Locate Plasmodium parasites and leukocytes.
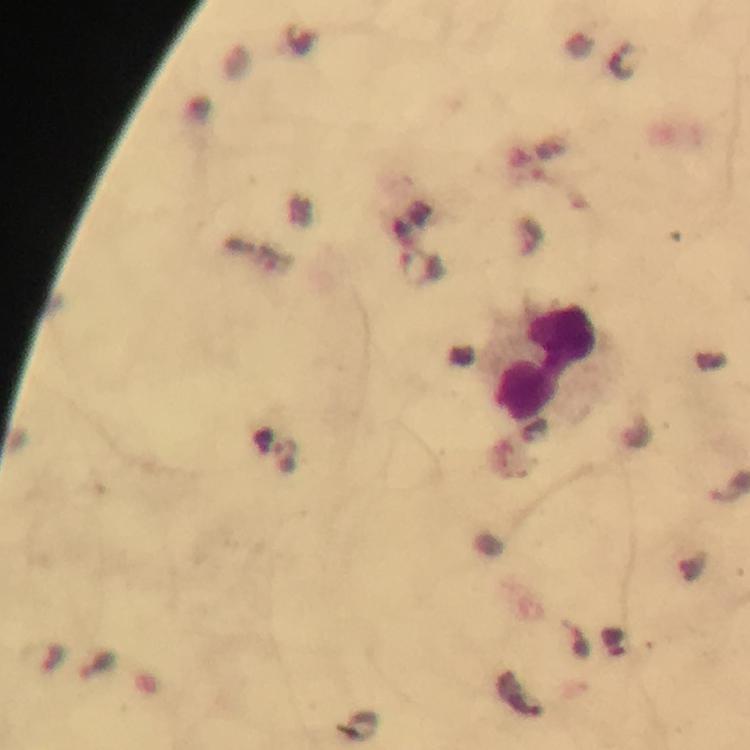
No Plasmodium parasites detected.
Approximate centers as {x, y} in pixels.
Leukocytes: {548, 363}.

Summary:
  - Context: from a malaria diagnostic workup
  - Immersion oil: used
  - Magnification: 100x
  - Image size: 750×750 pixels
  - Cropped from: one field of view
  - Preparation: thick smear
  - Capture: smartphone photograph through a microscope
  - Stain: Giemsa